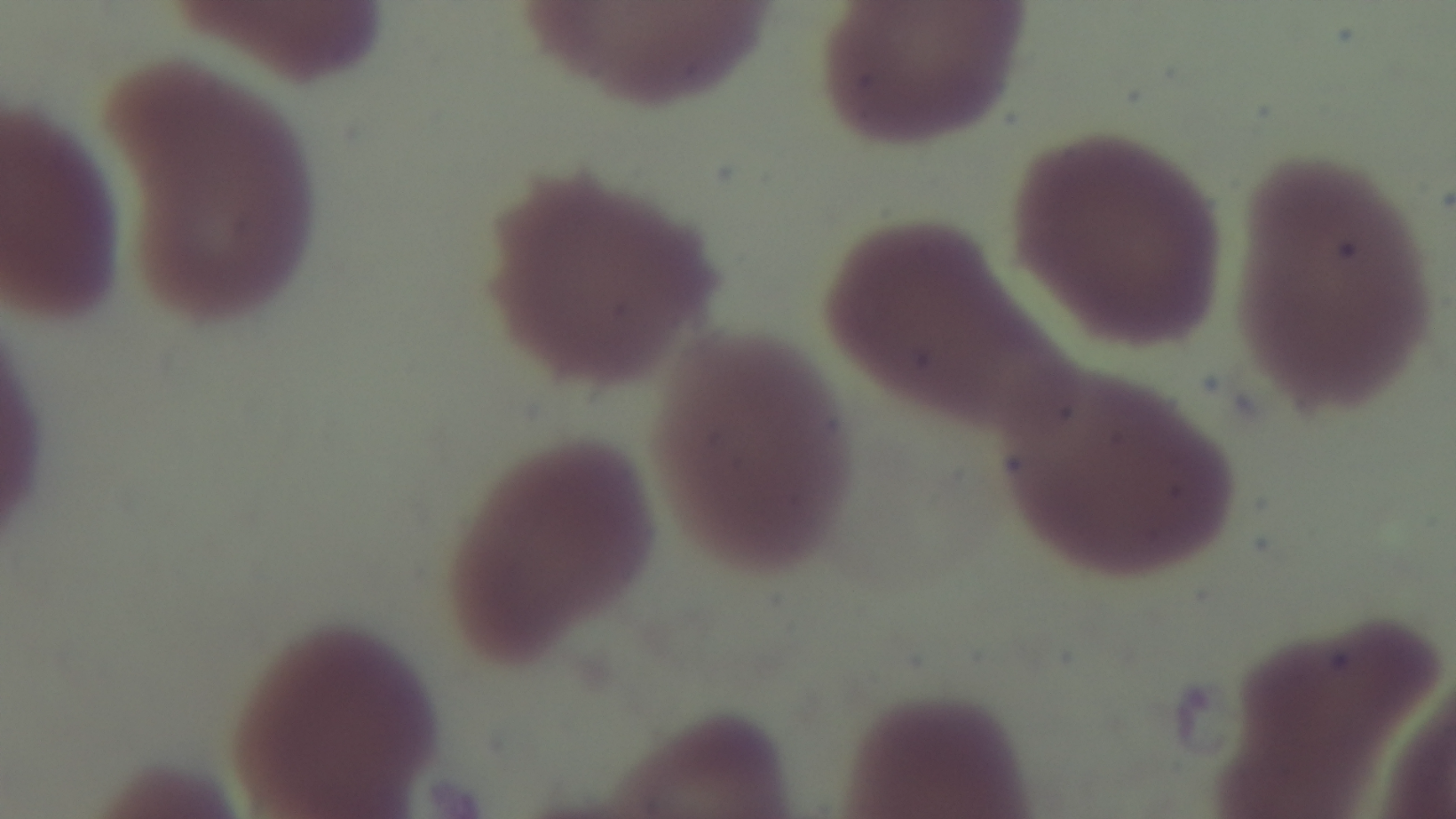

{
  "malaria_status": "negative",
  "objective": "100x oil immersion",
  "modality": "light microscopy",
  "field_of_view": "single",
  "preparation": "thin blood film",
  "stain": "Giemsa",
  "capture": "mounted 4K digital camera"
}